Report the malaria status of this cell.
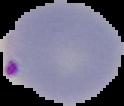

It is parasitized.

Image is 124×106 pixels. Segmented cell region on a black background. From a thin blood film.